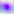
Summary:
  - Modality: photomicrograph
  - Identification: Toxoplasma gondii
  - Magnification: 400x